Assess this cell for malaria.
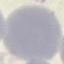

Uninfected.

image_type: automatically extracted cell patch, resized to 64 × 64 pixels
preparation: thin smear
capture: smartphone through the microscope eyepiece
stain: Giemsa